Assess the morphology of the erythrocytes.
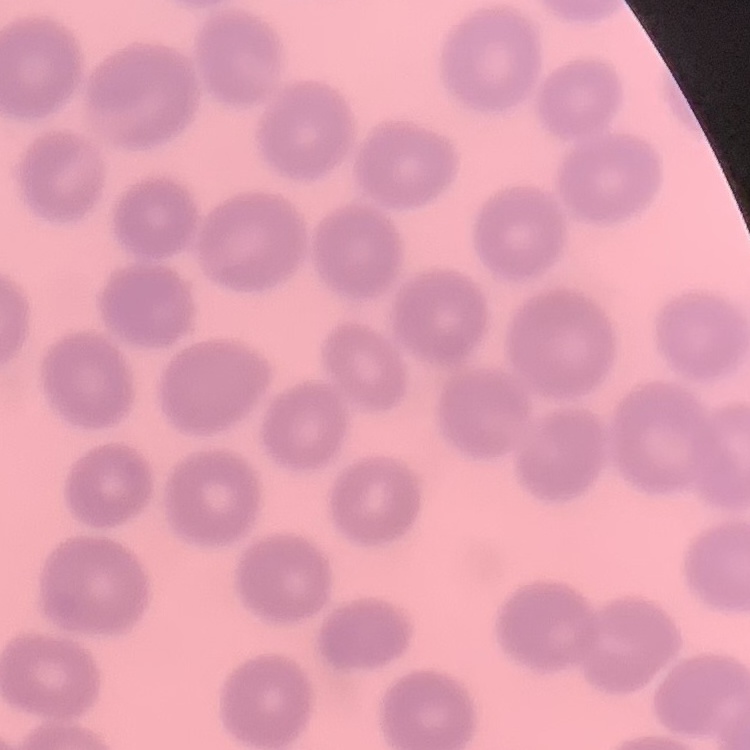
No rouleaux formation.

Field's or Giemsa stain. Thin blood smear. One tile cut from a larger photomicrograph.